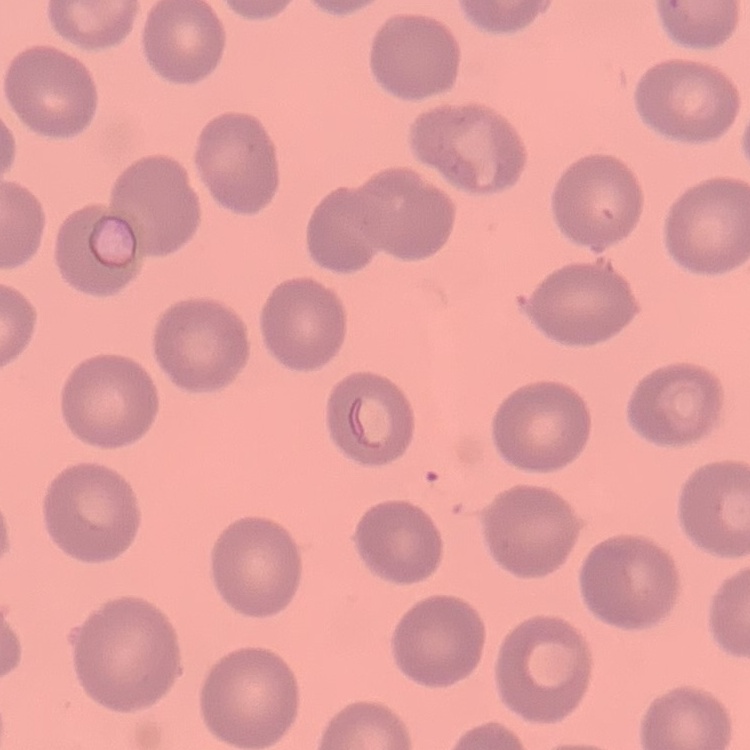
red blood cell morphology = no rouleaux formation
image type = square crop of a larger photomicrograph
preparation = thin blood smear
stain = Field's or Giemsa